Outline each Plasmodium falciparum-infected red blood cell.
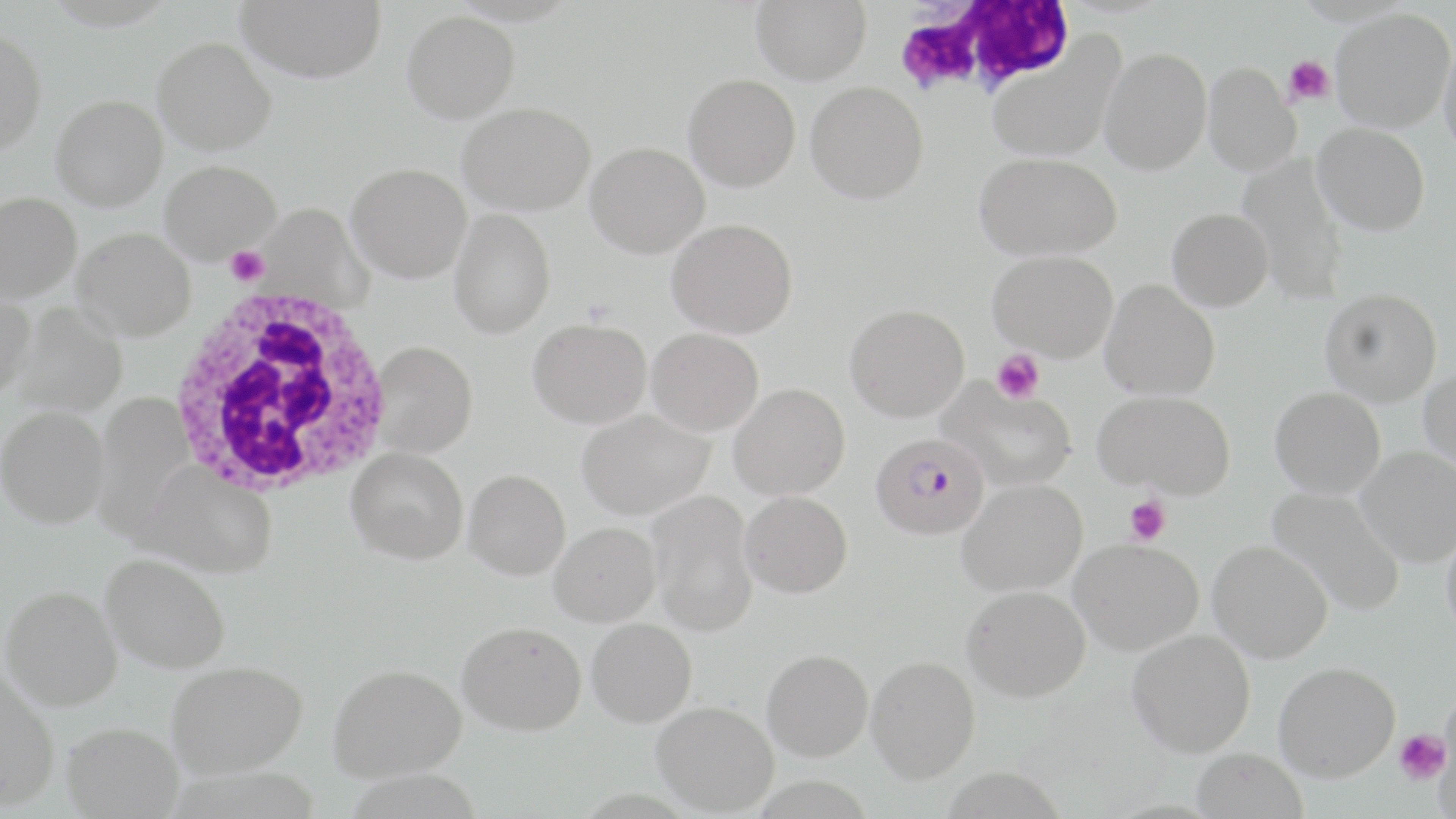

Approximate bounding boxes as (x1, y1, x2, y2) in pixels.
Plasmodium falciparum-infected red blood cells: (870, 432, 989, 540).

Uninfected red blood cell locations: (236, 0, 386, 83), (751, 0, 872, 84), (1331, 8, 1455, 132), (402, 10, 519, 123), (0, 28, 47, 153), (1438, 30, 1456, 158), (986, 34, 1126, 163), (153, 37, 276, 154), (1100, 46, 1212, 174), (1203, 62, 1300, 175), (683, 73, 801, 191), (806, 80, 929, 203), (51, 94, 167, 210), (458, 102, 595, 215), (1313, 122, 1430, 235), (586, 142, 709, 258), (974, 151, 1122, 261), (1237, 154, 1349, 302), (160, 160, 281, 262), (347, 162, 470, 282), (0, 191, 81, 302), (255, 204, 371, 310), (449, 208, 556, 338), (1167, 208, 1273, 311), (666, 218, 799, 339), (73, 227, 196, 340), (988, 249, 1118, 361), (1100, 280, 1220, 401), (1320, 287, 1442, 405), (0, 291, 35, 402), (10, 303, 129, 417), (845, 303, 969, 422), (528, 317, 652, 428), (647, 327, 764, 435), (373, 341, 476, 457), (1419, 368, 1456, 471), (938, 377, 1078, 491), (730, 383, 850, 499), (1270, 386, 1385, 498), (1095, 390, 1236, 498), (92, 392, 191, 540), (0, 405, 109, 528), (577, 409, 714, 519), (1357, 446, 1456, 567), (347, 447, 468, 564), (131, 463, 278, 578), (464, 469, 570, 580), (957, 478, 1087, 596), (1268, 487, 1406, 617), (647, 490, 759, 637), (740, 491, 852, 597), (549, 522, 660, 626), (1441, 524, 1456, 642), (1070, 538, 1204, 655), (1208, 539, 1333, 663), (101, 553, 231, 673), (1, 585, 123, 710), (962, 585, 1090, 701), (587, 618, 697, 726), (457, 621, 586, 734), (1127, 629, 1256, 756), (762, 648, 873, 761), (866, 655, 980, 783), (166, 661, 307, 776), (1274, 662, 1400, 782), (328, 663, 466, 780), (0, 667, 60, 810), (652, 701, 779, 815), (61, 722, 184, 818), (1192, 748, 1308, 819). Platelet locations: (1285, 56, 1334, 105), (226, 246, 269, 286), (993, 349, 1044, 403), (1124, 495, 1171, 545), (1393, 729, 1449, 784). White blood cell locations: (894, 1, 1076, 98), (163, 285, 397, 499). Slide-level diagnosis: Plasmodium falciparum. Single field of view. Optical microscopy. May-Grünwald-Giemsa stain. 1000x magnification. Image is 1456×819 pixels. Thin blood film.